Comment on the morphology of the erythrocytes.
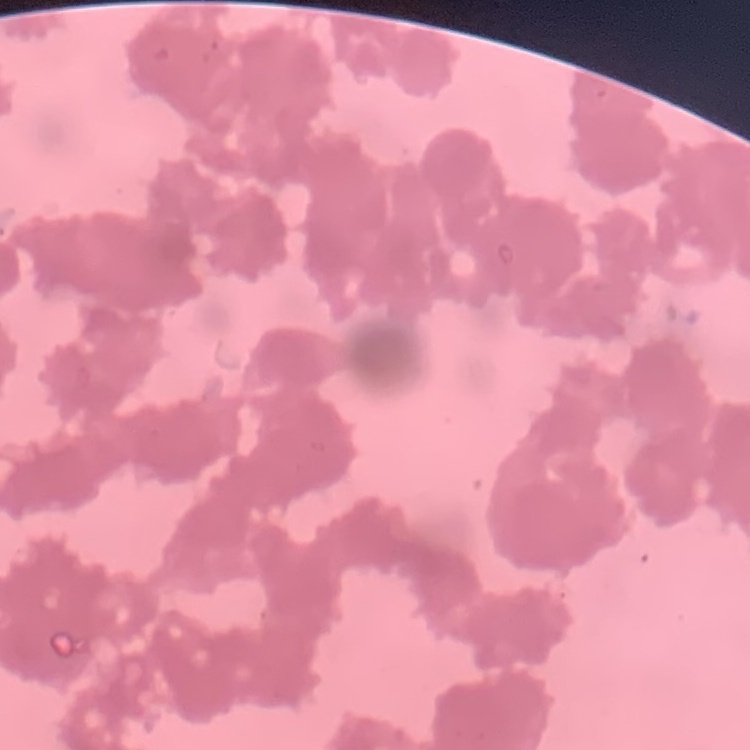

Rouleaux formation.

One tile cut from a larger photomicrograph. Stained with either Field's or Giemsa. Thin blood film.